Assess this cell for malaria.
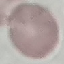
It is uninfected.

Summary:
  - Image type: cell patch, automatically extracted from a larger field of view and resized to 64 × 64 pixels
  - Capture: smartphone through the microscope eyepiece
  - Preparation: thin blood film
  - Stain: Giemsa